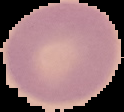 From a thin blood film. Image is 124×112 pixels. Result: no malaria parasites seen. Cell region segmented out of the field of view; the surrounding area is masked to black.